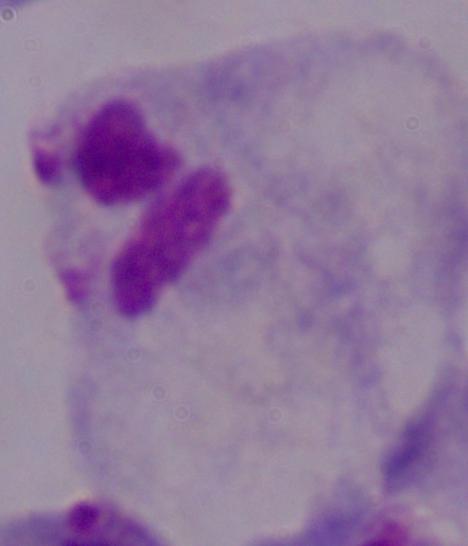
A trichomonad is seen. Captured at 1000x magnification. Micrograph.